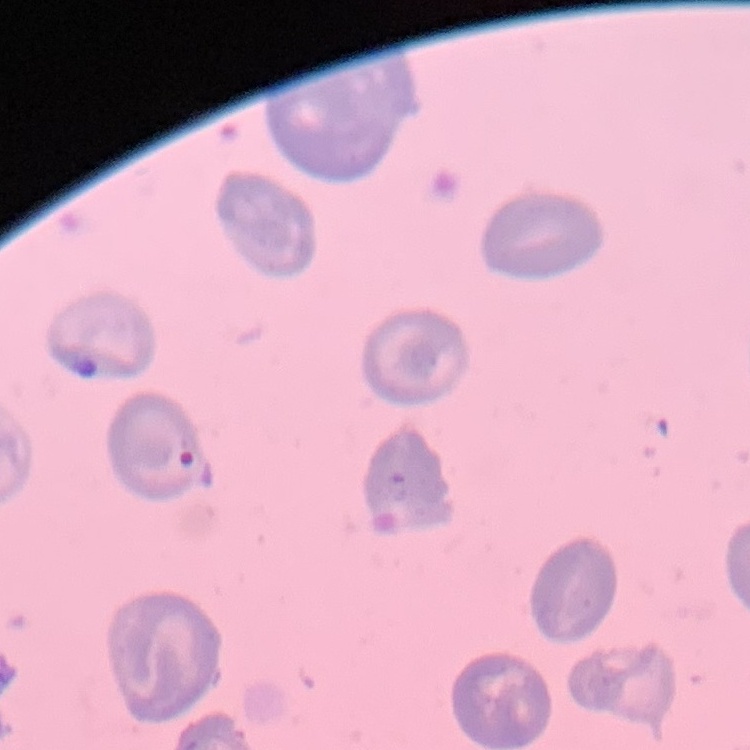

red_blood_cell_morphology: no rouleaux formation
stain: Field's or Giemsa
image_type: one tile cut from a larger photomicrograph
preparation: thin blood film